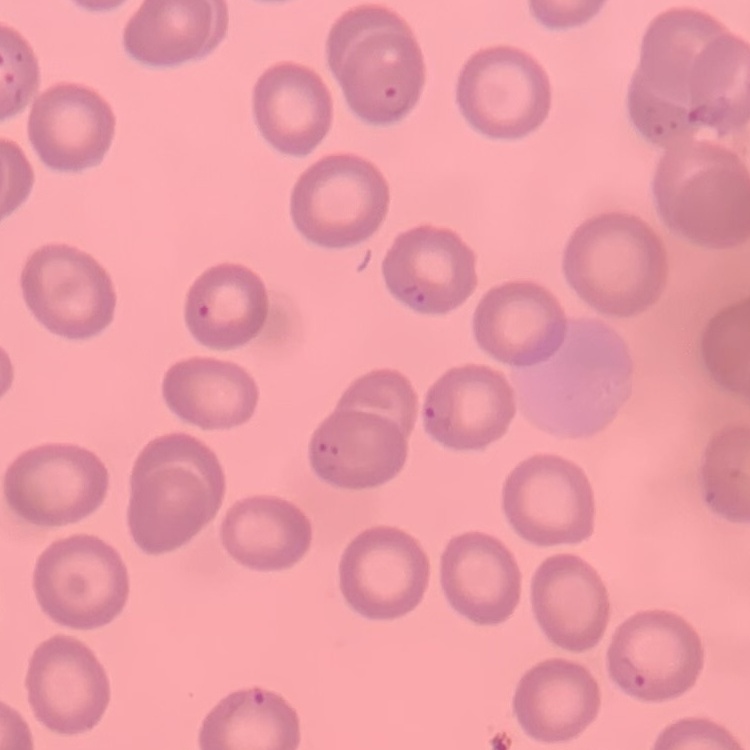
red blood cell morphology = no rouleaux formation
stain = Field's or Giemsa
image type = square crop of a larger photomicrograph
preparation = thin blood film